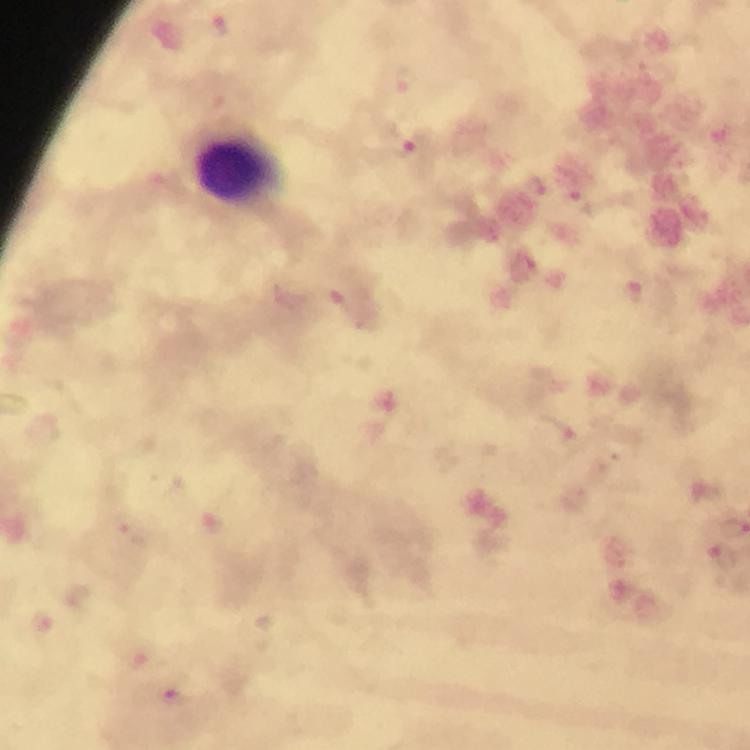

Approximate object centers, in pixels from the top-left corner. Plasmodium parasite locations: (x=219, y=25), (x=406, y=81), (x=410, y=147), (x=536, y=185), (x=582, y=203), (x=634, y=290), (x=560, y=429), (x=129, y=528), (x=724, y=556), (x=40, y=620), (x=173, y=693). Leukocyte locations: (x=237, y=166). Giemsa-stained preparation. Photographed with a smartphone mounted on the microscope. At 100x magnification. Image is 750×750 pixels. Immersion oil applied. Thick blood smear. A crop from one field of view. From a malaria diagnostic workup.